Outline platelets.
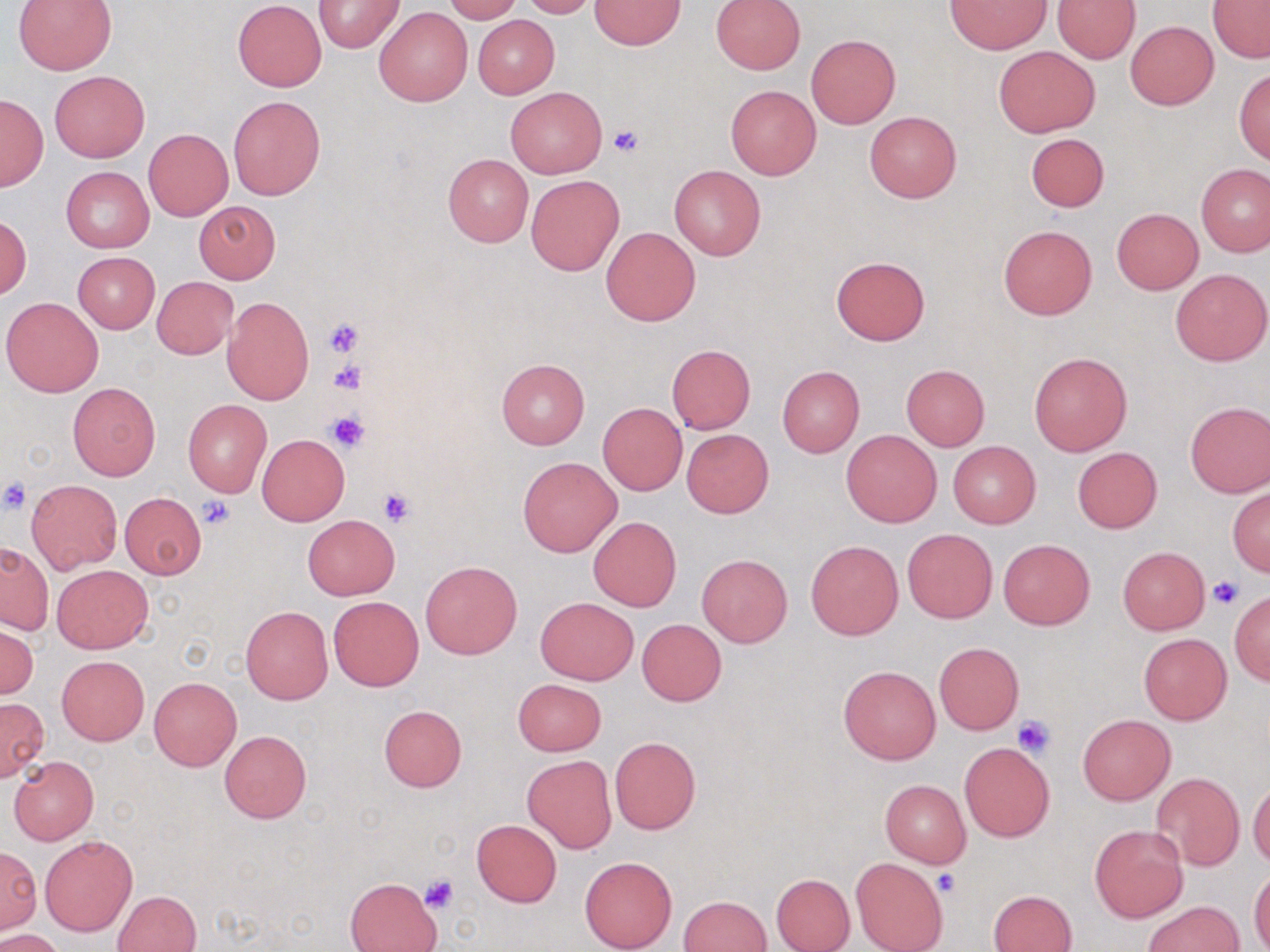
Approximate bounding boxes as [x1, y1, x2, y2] in pixels.
Platelets: [609, 124, 642, 155], [324, 317, 365, 356], [329, 360, 366, 396], [326, 412, 369, 454], [0, 477, 31, 513], [377, 486, 416, 525], [197, 495, 236, 529], [1208, 576, 1243, 610], [1013, 714, 1055, 758], [935, 871, 960, 897], [419, 874, 460, 914].

slide-level diagnosis = no evidence of blood parasites
uninfected red blood cell locations = approximate bounding boxes as [x1, y1, x2, y2] in pixels: [443, 0, 519, 22], [520, 0, 598, 18], [710, 0, 805, 74], [947, 0, 1050, 54], [1053, 0, 1140, 63], [1206, 0, 1270, 63], [13, 1, 116, 74], [233, 1, 327, 92], [315, 1, 404, 52], [590, 1, 686, 49], [373, 7, 472, 106], [472, 14, 559, 98], [1125, 21, 1219, 111], [806, 34, 900, 129], [993, 45, 1100, 137], [1234, 68, 1270, 164], [50, 71, 149, 161], [725, 83, 821, 179], [507, 86, 606, 178], [1, 93, 48, 191], [229, 95, 325, 199], [864, 111, 962, 203], [144, 128, 232, 220], [1025, 133, 1109, 212], [443, 154, 533, 247], [1196, 163, 1270, 257], [670, 165, 765, 260], [61, 167, 153, 253], [526, 174, 623, 274], [194, 201, 281, 284], [1111, 208, 1203, 294], [1, 216, 31, 299], [601, 225, 700, 326], [999, 225, 1097, 320], [72, 251, 159, 333], [830, 255, 931, 345], [1171, 268, 1270, 365], [152, 277, 237, 358], [222, 295, 314, 404], [2, 297, 104, 397], [666, 344, 755, 434], [1029, 352, 1131, 456], [496, 358, 589, 449], [900, 364, 990, 451], [777, 367, 865, 456], [68, 382, 160, 480], [183, 399, 271, 496], [1185, 401, 1270, 498], [599, 402, 686, 495], [681, 428, 773, 517], [842, 430, 942, 528], [257, 434, 349, 525], [948, 440, 1041, 528], [1072, 447, 1163, 533], [518, 457, 622, 557], [27, 479, 122, 573], [1227, 486, 1269, 576], [119, 493, 207, 579], [303, 515, 399, 599], [588, 516, 682, 612], [902, 527, 998, 623], [999, 538, 1094, 629], [806, 540, 903, 640], [1, 541, 53, 635], [1117, 546, 1209, 634], [697, 555, 792, 646], [420, 559, 522, 659], [51, 563, 153, 653], [1228, 592, 1270, 685], [328, 596, 423, 691], [536, 596, 638, 684], [241, 605, 333, 704], [636, 619, 726, 706], [1, 622, 38, 702], [1139, 633, 1232, 725], [934, 642, 1023, 734], [56, 655, 149, 746], [838, 665, 940, 764], [148, 677, 241, 770], [512, 679, 605, 756], [0, 697, 49, 782], [379, 705, 467, 792], [1078, 715, 1175, 804], [219, 730, 312, 823], [610, 736, 701, 835], [959, 743, 1055, 841], [8, 755, 99, 846], [522, 755, 617, 854], [1151, 772, 1244, 870], [1248, 775, 1270, 867], [879, 778, 971, 867], [472, 819, 562, 907], [1089, 824, 1188, 924], [40, 835, 137, 936], [1, 849, 39, 937], [580, 855, 678, 952], [852, 857, 948, 952], [1248, 868, 1270, 952], [770, 873, 855, 952], [344, 878, 439, 952], [113, 889, 203, 952], [990, 889, 1077, 952], [680, 895, 771, 951], [1143, 901, 1246, 952], [0, 929, 67, 952]
image size = 1270×952 pixels
stain = May-Grünwald-Giemsa
field of view = single
magnification = 1000x
preparation = thin blood film
modality = optical microscopy